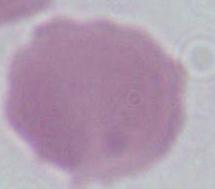
A red blood cell is shown. Photomicrograph. 1000x magnification.